Point out each leukocyte.
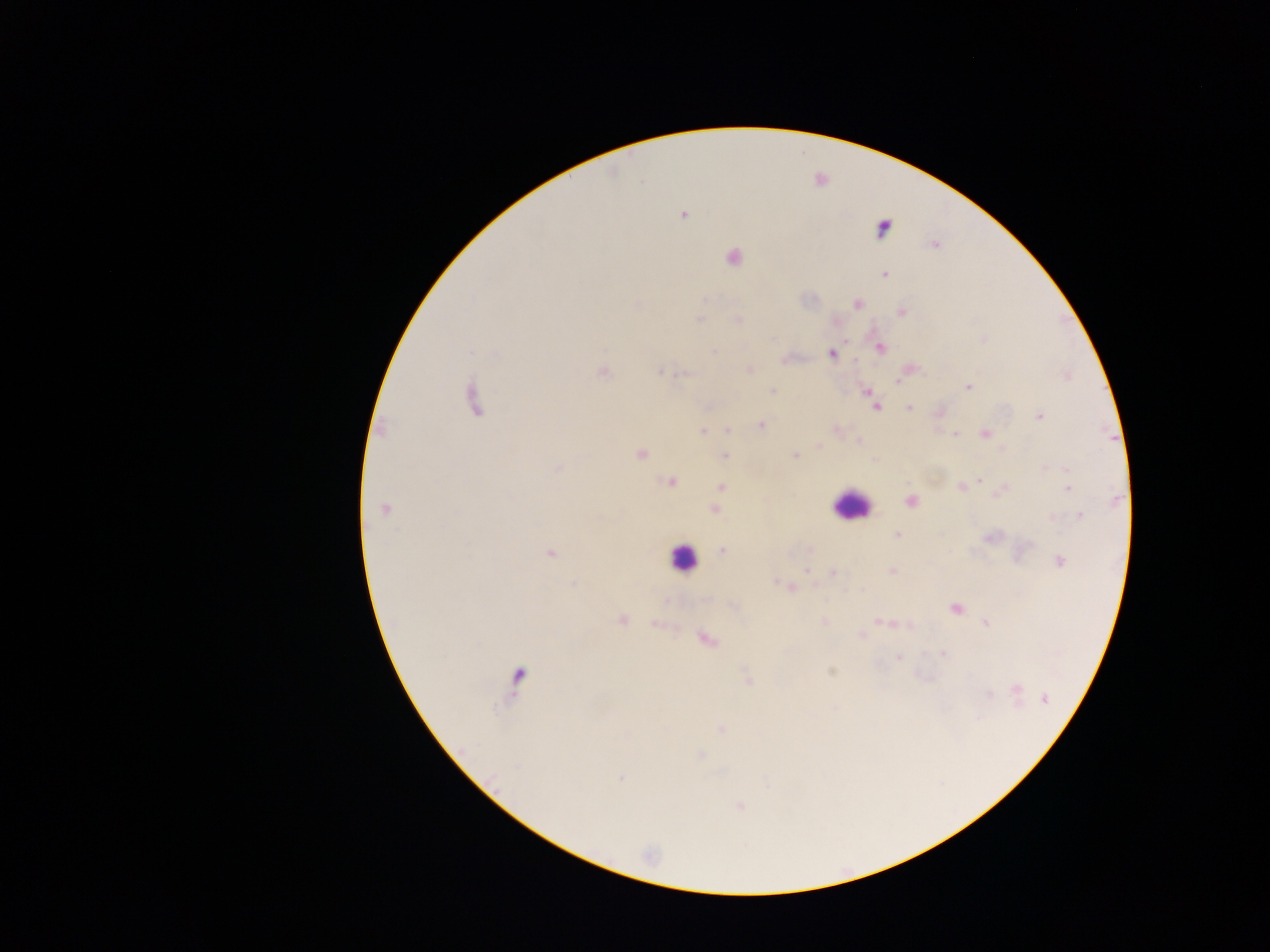
Approximate centers as (x, y) in pixels.
Leukocytes: (851, 505), (682, 559).

{
  "malaria_parasite_locations": "approximate centers as (x, y) in pixels: (684, 215), (883, 227), (933, 244), (732, 257), (884, 274), (856, 303), (900, 312), (699, 320), (738, 320), (878, 347), (830, 353), (786, 358), (749, 369), (907, 370), (602, 371), (660, 371), (1067, 376), (968, 387), (772, 391), (866, 391), (472, 398), (872, 402), (875, 407), (908, 407), (938, 413), (1039, 415), (759, 425), (836, 429), (702, 430), (727, 431), (985, 433), (956, 434), (858, 442), (818, 445), (641, 453), (724, 456), (794, 456), (557, 469), (1066, 470), (980, 480), (670, 481), (721, 486), (960, 486), (1067, 488), (719, 491), (1000, 492), (910, 501), (384, 509), (714, 510), (1079, 515), (1051, 518), (897, 534), (722, 550), (810, 550), (549, 552), (1059, 561), (892, 571), (832, 572), (774, 581), (574, 583), (789, 588), (955, 607), (621, 620), (880, 622), (985, 622), (823, 623), (655, 624), (908, 625), (862, 635), (705, 639), (941, 653), (898, 657), (830, 671), (516, 676), (748, 680), (1015, 689), (1045, 699), (721, 728), (700, 755), (622, 779), (740, 805)",
  "country": "Ghana",
  "preparation": "thick blood smear",
  "capture": "mobile-phone photograph through a microscope",
  "field_of_view": "single",
  "image_size": "1270×952 pixels"
}